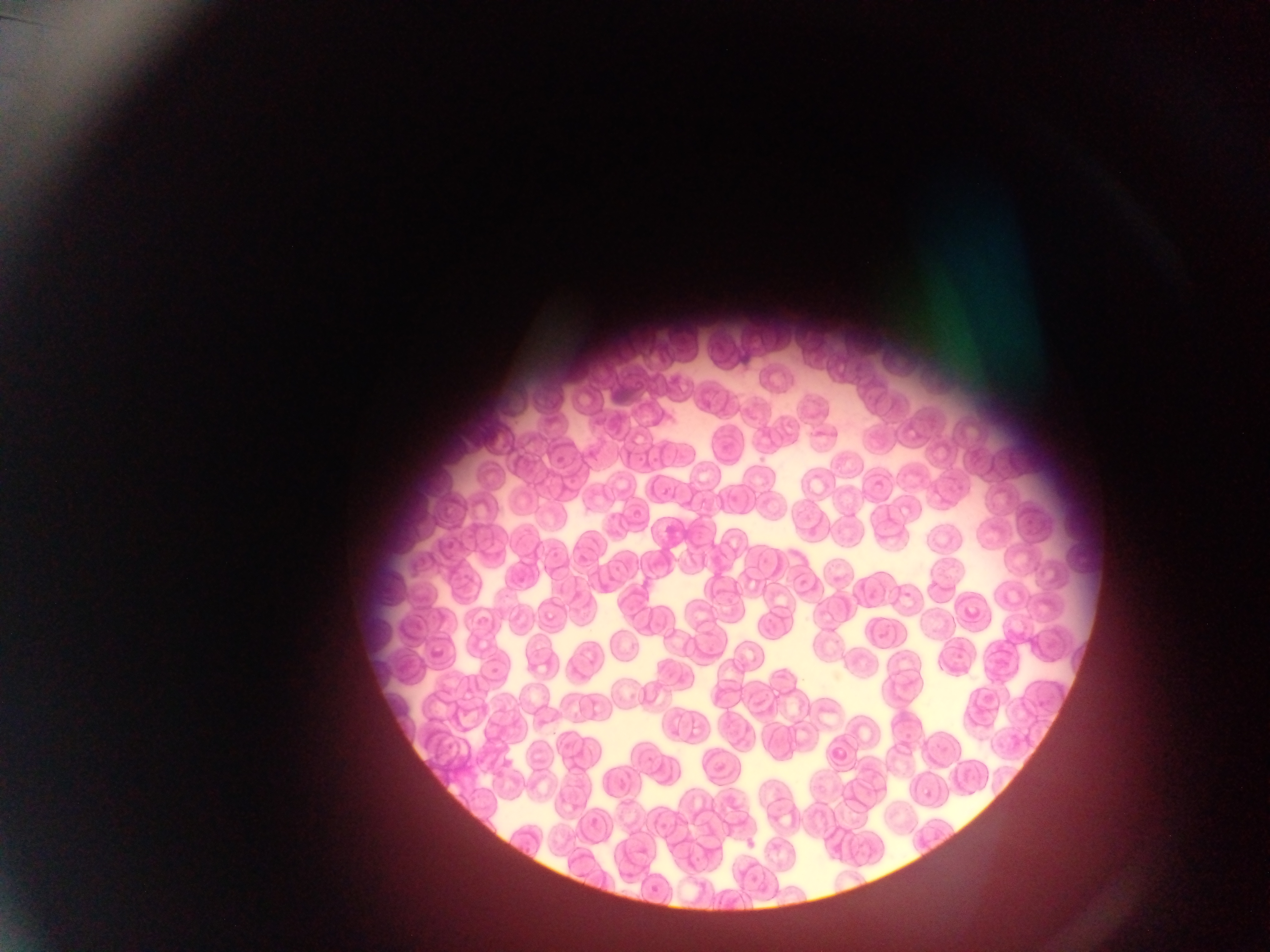

Approximate bounding boxes as (left, top, right, bottom) in pixels. Malaria parasite locations: (662, 486, 676, 502), (922, 786, 938, 803), (635, 842, 652, 861). Mobile-phone photograph taken through the microscope. Sample from Ghana. Image is 1270×952 pixels. One field of view. Thin blood film.